Classify this cell by malaria status.
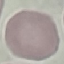
It is uninfected.

Summary:
  - Stain: Giemsa
  - Image type: cell patch, automatically extracted from a larger field of view and resized to 64 × 64 pixels
  - Capture: smartphone through the microscope eyepiece
  - Preparation: thin smear